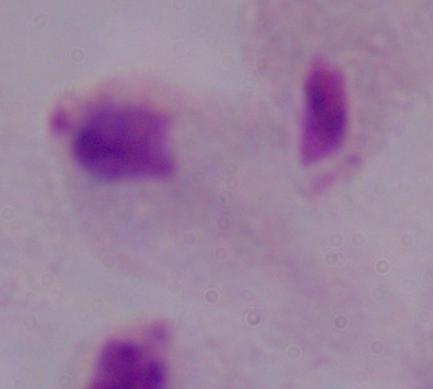
Summary:
  - Modality: photomicrograph
  - Magnification: 1000x
  - Identification: trichomonad